Locate and identify every blood parasite.
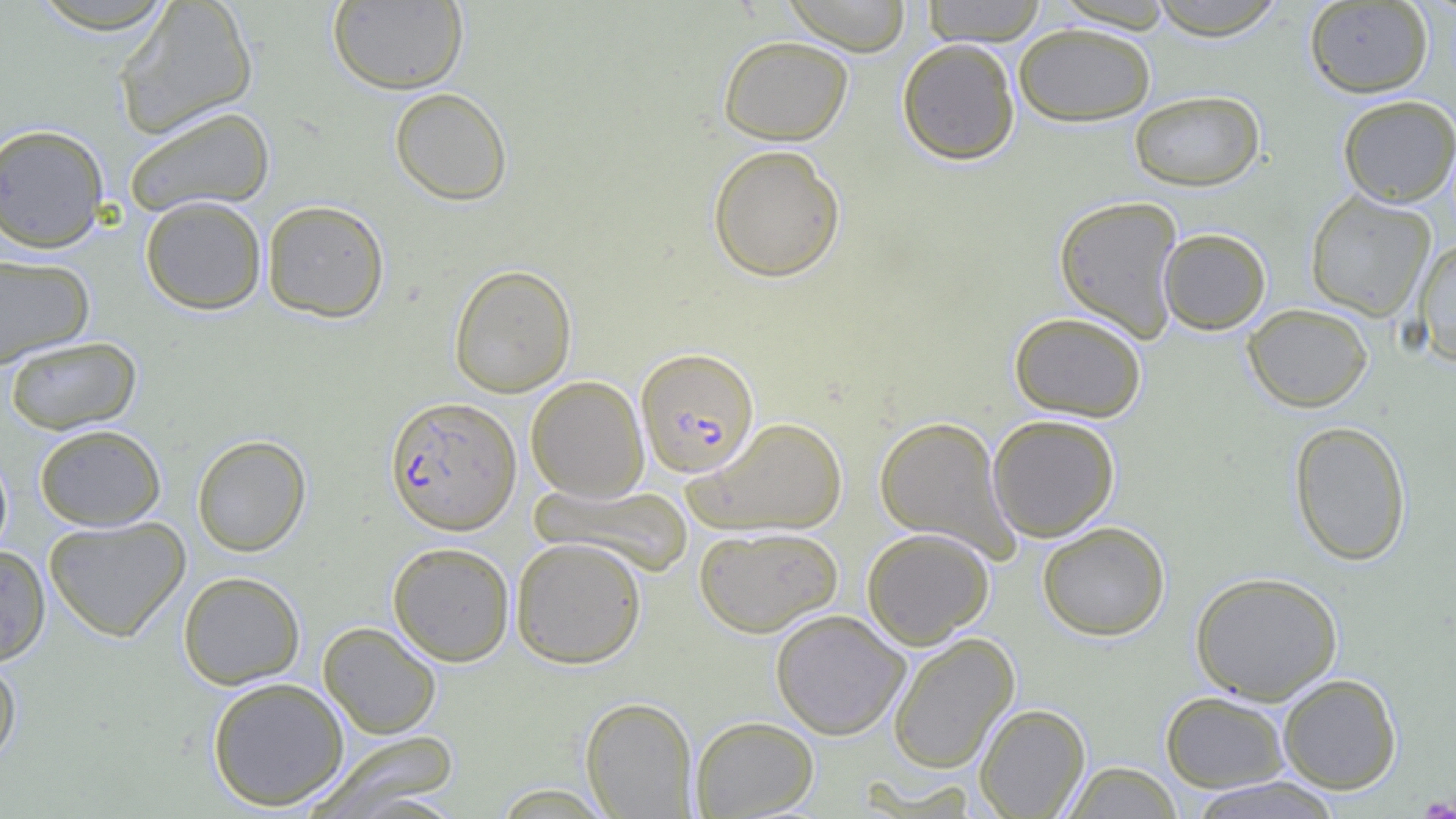

Approximate bounding boxes as (x1, y1, x2, y2) in pixels.
Plasmodium falciparum-infected red blood cells: (639, 351, 764, 483), (384, 396, 522, 535).
No Plasmodium ovale, Plasmodium malariae, Plasmodium vivax, Babesia divergens, or Trypanosoma brucei observed.

Summary:
  - Uninfected red blood cell locations: (327, 0, 468, 94), (782, 0, 911, 55), (1147, 0, 1288, 39), (25, 1, 184, 38), (113, 1, 260, 137), (921, 1, 1048, 46), (1303, 1, 1434, 97), (1013, 22, 1157, 126), (718, 35, 853, 145), (897, 38, 1020, 165), (390, 87, 513, 206), (1128, 89, 1265, 192), (1337, 94, 1456, 207), (122, 106, 276, 218), (0, 123, 110, 253), (707, 144, 846, 283), (1304, 190, 1436, 321), (1053, 194, 1184, 342), (140, 195, 267, 314), (262, 199, 390, 322), (1158, 228, 1271, 334), (1413, 237, 1456, 367), (0, 253, 95, 368), (448, 264, 577, 397), (1243, 304, 1373, 412), (1009, 310, 1147, 422), (4, 336, 141, 434), (526, 375, 649, 502), (987, 414, 1120, 542), (874, 415, 1018, 559), (686, 416, 848, 536), (1289, 420, 1412, 566), (34, 423, 166, 531), (192, 434, 311, 556), (0, 449, 13, 564), (530, 482, 693, 577), (43, 516, 190, 642), (1037, 521, 1170, 641), (693, 525, 844, 637), (861, 527, 994, 649), (511, 536, 647, 668), (387, 541, 515, 666), (0, 545, 51, 666), (1190, 570, 1343, 704), (177, 571, 305, 689), (770, 609, 910, 740), (318, 621, 442, 739), (887, 632, 1020, 774), (0, 656, 22, 770), (1278, 673, 1402, 794), (207, 677, 349, 811), (1160, 690, 1290, 792), (580, 696, 699, 818), (975, 702, 1090, 818), (690, 715, 820, 818), (305, 731, 461, 818), (1060, 761, 1183, 818), (1186, 777, 1345, 819)
  - Slide-level diagnosis: Plasmodium falciparum
  - Modality: optical microscopy
  - Magnification: 1000x
  - Image size: 1456×819 pixels
  - Preparation: thin blood smear
  - Field of view: one of a larger specimen